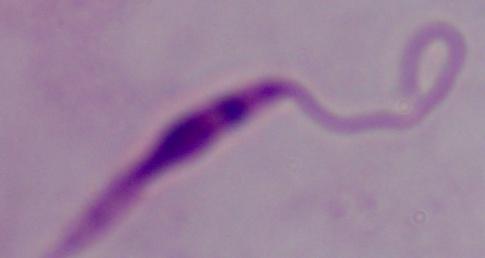

Summary:
  - Magnification: 1000x
  - Identification: Leishmania
  - Modality: photomicrograph